Classify this cell by malaria status.
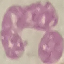

Uninfected.

Summary:
  - Image type: automatically extracted cell patch, resized to 64 × 64 pixels
  - Stain: Giemsa
  - Capture: smartphone through the microscope eyepiece
  - Preparation: thin blood film